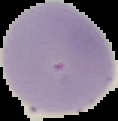

image type = cell region segmented out of the field of view; surrounding area masked to black
malaria status = uninfected
image size = 118×121 pixels
preparation = thin blood smear